State which parasite is depicted.
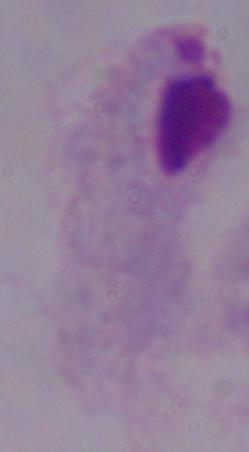
A trichomonad.

modality = photomicrograph
magnification = 1000x